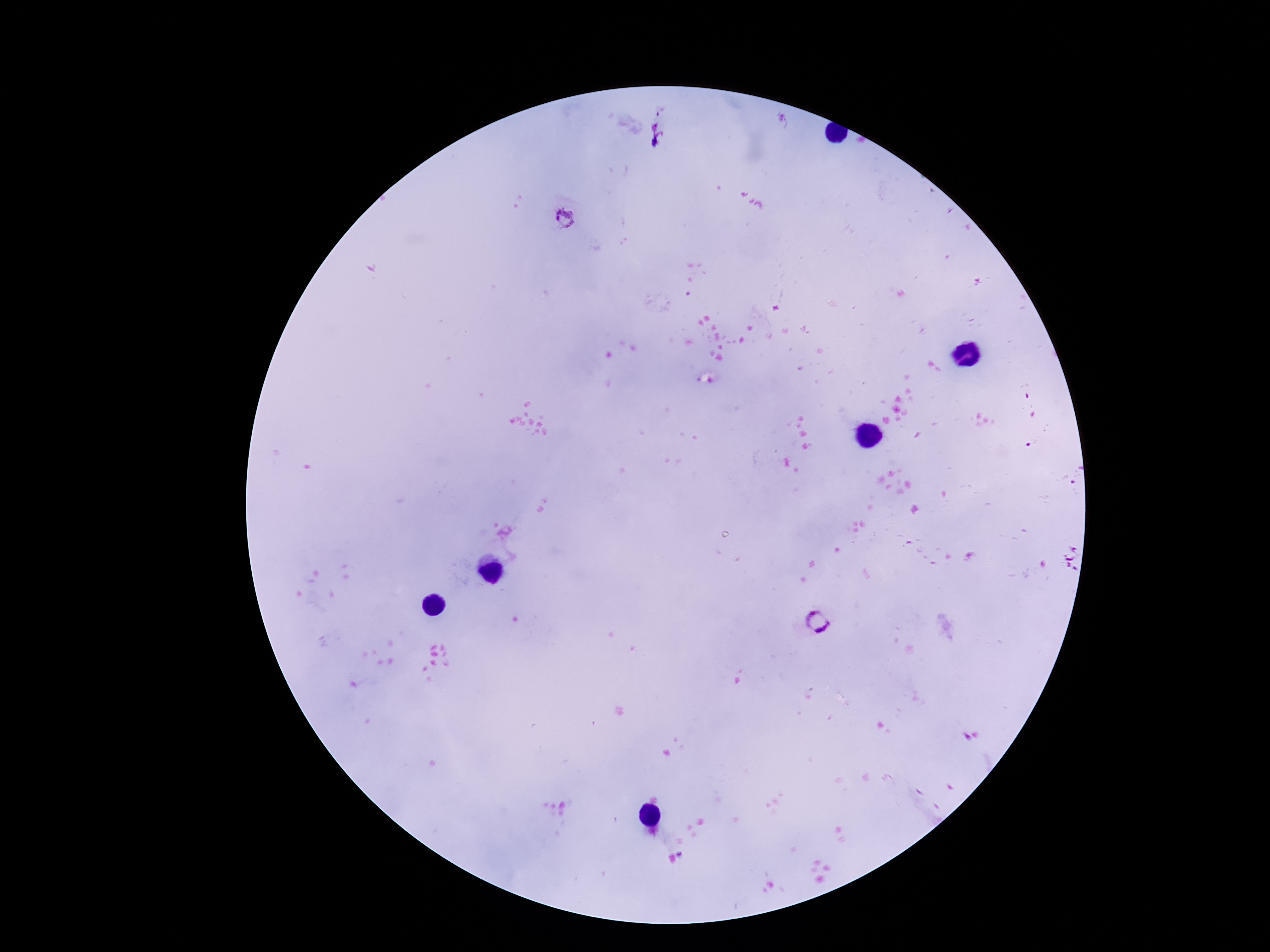

field of view = one from this slide
Plasmodium parasite locations = approximate centers as (x, y) in pixels: (564, 217), (1069, 557), (815, 623)
stain = Giemsa
patient malaria status = positive
magnification = 100x
preparation = thick blood smear
capture = smartphone camera through the microscope eyepiece
image size = 1270×952 pixels